Classify this cell by malaria status.
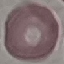

Uninfected.

Summary:
  - Stain: Giemsa
  - Preparation: thin smear
  - Capture: smartphone through the microscope eyepiece
  - Image type: automatically extracted cell patch, resized to 64 × 64 pixels